Locate every malaria parasite.
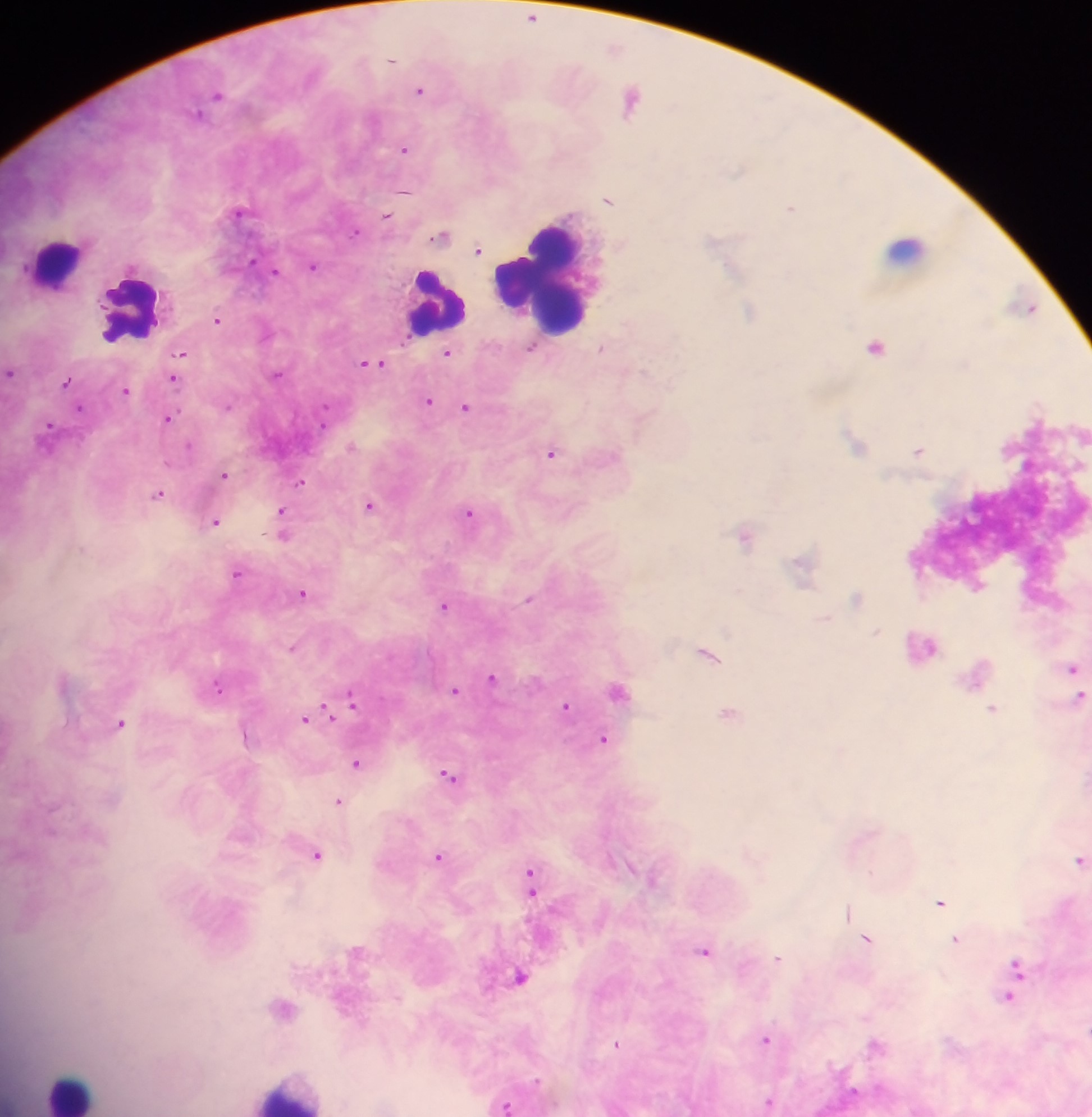
Approximate centers as [x, y] in pixels.
Malaria parasites: [532, 16], [392, 60], [420, 91], [219, 95], [632, 100], [198, 113], [404, 150], [404, 191], [609, 201], [791, 206], [387, 215], [356, 232], [439, 235], [479, 250], [252, 262], [315, 266], [731, 266], [275, 271], [1031, 309], [750, 310], [218, 319], [876, 346], [531, 350], [182, 353], [449, 353], [372, 362], [966, 365], [11, 373], [278, 374], [173, 377], [65, 381], [125, 390], [429, 402], [1037, 404], [326, 407], [466, 409], [169, 417], [50, 425], [324, 426], [856, 441], [190, 445], [919, 451], [553, 454], [225, 476], [301, 483], [159, 494], [371, 508], [284, 515], [469, 516], [217, 523], [284, 525], [744, 537], [304, 594], [529, 600], [443, 605], [494, 678], [219, 685], [456, 691], [619, 692], [352, 703], [567, 706], [329, 713], [729, 714], [305, 719], [606, 741], [358, 764], [449, 775], [341, 801], [318, 856], [437, 857], [1078, 860], [528, 874], [531, 881], [941, 902], [848, 911], [956, 938], [869, 940], [706, 951], [777, 958], [1014, 986], [766, 1039], [768, 1101], [507, 1106].

Leukocyte locations: [900, 250], [57, 259], [546, 282], [432, 295], [126, 311], [63, 1087]. Image is 1092×1117 pixels. One field of view. Photographed through a microscope with a mobile-phone camera. Thick blood smear. Collected in Ghana.